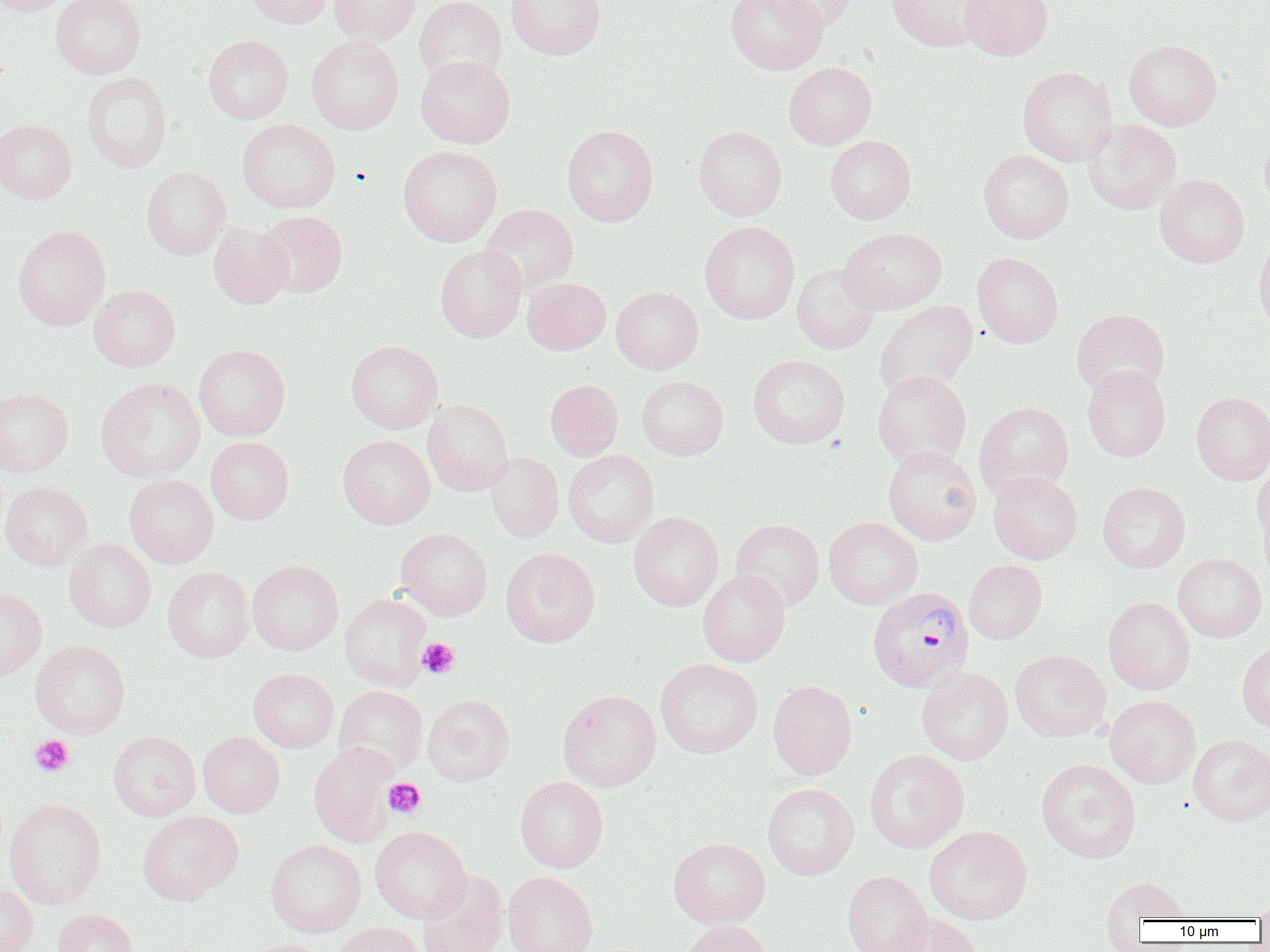
slide-level diagnosis = Plasmodium vivax
image size = 1270×952 pixels
preparation = thin blood smear
modality = optical microscopy
magnification = 1000x
Plasmodium vivax-infected red blood cell locations = approximate bounding boxes as named x1/y1/x2/y2 corners in pixels: (x1=867, y1=586, x2=974, y2=692)
uninfected red blood cell locations = approximate bounding boxes as named x1/y1/x2/y2 corners in pixels: (x1=0, y1=0, x2=74, y2=15), (x1=51, y1=0, x2=146, y2=78), (x1=245, y1=0, x2=334, y2=28), (x1=330, y1=0, x2=421, y2=45), (x1=414, y1=0, x2=506, y2=85), (x1=505, y1=0, x2=605, y2=60), (x1=726, y1=0, x2=828, y2=74), (x1=766, y1=0, x2=858, y2=31), (x1=887, y1=0, x2=992, y2=51), (x1=960, y1=0, x2=1053, y2=60), (x1=203, y1=35, x2=293, y2=124), (x1=307, y1=35, x2=404, y2=134), (x1=1124, y1=39, x2=1222, y2=130), (x1=415, y1=55, x2=515, y2=148), (x1=784, y1=61, x2=876, y2=149), (x1=1017, y1=66, x2=1117, y2=166), (x1=82, y1=72, x2=172, y2=172), (x1=0, y1=119, x2=77, y2=202), (x1=237, y1=119, x2=340, y2=213), (x1=1084, y1=119, x2=1182, y2=214), (x1=562, y1=124, x2=658, y2=225), (x1=694, y1=126, x2=787, y2=221), (x1=1260, y1=128, x2=1270, y2=215), (x1=825, y1=135, x2=916, y2=223), (x1=398, y1=145, x2=502, y2=247), (x1=978, y1=149, x2=1074, y2=243), (x1=141, y1=165, x2=231, y2=260), (x1=1155, y1=174, x2=1249, y2=267), (x1=481, y1=203, x2=578, y2=295), (x1=256, y1=211, x2=347, y2=297), (x1=699, y1=220, x2=800, y2=324), (x1=208, y1=222, x2=293, y2=309), (x1=13, y1=225, x2=110, y2=330), (x1=838, y1=227, x2=947, y2=314), (x1=1253, y1=233, x2=1270, y2=338), (x1=435, y1=245, x2=527, y2=342), (x1=972, y1=252, x2=1063, y2=347), (x1=792, y1=263, x2=880, y2=354), (x1=523, y1=277, x2=611, y2=354), (x1=89, y1=284, x2=180, y2=371), (x1=611, y1=286, x2=703, y2=374), (x1=875, y1=300, x2=978, y2=397), (x1=1071, y1=309, x2=1170, y2=398), (x1=346, y1=340, x2=443, y2=433), (x1=194, y1=344, x2=290, y2=441), (x1=748, y1=354, x2=850, y2=448), (x1=1082, y1=365, x2=1171, y2=461), (x1=872, y1=370, x2=971, y2=469), (x1=636, y1=376, x2=728, y2=459), (x1=96, y1=377, x2=205, y2=481), (x1=545, y1=379, x2=623, y2=461), (x1=0, y1=387, x2=74, y2=477), (x1=1191, y1=391, x2=1270, y2=484), (x1=422, y1=399, x2=513, y2=495), (x1=975, y1=401, x2=1073, y2=497), (x1=338, y1=435, x2=436, y2=528), (x1=206, y1=437, x2=294, y2=524), (x1=883, y1=445, x2=981, y2=545), (x1=563, y1=450, x2=659, y2=547), (x1=485, y1=451, x2=564, y2=543), (x1=1253, y1=458, x2=1269, y2=547), (x1=988, y1=471, x2=1082, y2=563), (x1=124, y1=474, x2=219, y2=568), (x1=0, y1=481, x2=93, y2=570), (x1=1097, y1=482, x2=1190, y2=572), (x1=1258, y1=497, x2=1270, y2=587), (x1=628, y1=511, x2=724, y2=611), (x1=823, y1=517, x2=922, y2=608), (x1=731, y1=518, x2=824, y2=611), (x1=396, y1=528, x2=492, y2=620), (x1=64, y1=538, x2=156, y2=632), (x1=500, y1=547, x2=600, y2=647), (x1=1173, y1=552, x2=1267, y2=642), (x1=247, y1=559, x2=343, y2=655), (x1=964, y1=559, x2=1047, y2=644), (x1=163, y1=566, x2=253, y2=662), (x1=698, y1=569, x2=791, y2=666), (x1=0, y1=587, x2=47, y2=681), (x1=339, y1=593, x2=432, y2=690), (x1=1104, y1=596, x2=1195, y2=695), (x1=1237, y1=638, x2=1270, y2=733), (x1=30, y1=639, x2=131, y2=738), (x1=1010, y1=649, x2=1111, y2=742), (x1=655, y1=658, x2=763, y2=758), (x1=916, y1=667, x2=1013, y2=764), (x1=249, y1=668, x2=338, y2=752), (x1=768, y1=680, x2=857, y2=779), (x1=334, y1=685, x2=428, y2=775), (x1=558, y1=689, x2=661, y2=791), (x1=423, y1=694, x2=515, y2=786), (x1=1105, y1=694, x2=1200, y2=788), (x1=108, y1=731, x2=200, y2=821), (x1=198, y1=732, x2=285, y2=817), (x1=1187, y1=734, x2=1270, y2=826), (x1=309, y1=743, x2=397, y2=847), (x1=865, y1=749, x2=969, y2=853), (x1=1036, y1=759, x2=1140, y2=863), (x1=515, y1=776, x2=608, y2=873), (x1=763, y1=783, x2=859, y2=880), (x1=5, y1=798, x2=106, y2=908), (x1=137, y1=811, x2=242, y2=905), (x1=925, y1=825, x2=1032, y2=924), (x1=370, y1=826, x2=471, y2=923), (x1=668, y1=837, x2=770, y2=928), (x1=266, y1=839, x2=366, y2=937), (x1=416, y1=870, x2=509, y2=952), (x1=503, y1=871, x2=598, y2=952), (x1=842, y1=871, x2=933, y2=952), (x1=1100, y1=875, x2=1193, y2=927), (x1=0, y1=882, x2=38, y2=952), (x1=1254, y1=892, x2=1270, y2=923), (x1=52, y1=907, x2=139, y2=952), (x1=884, y1=913, x2=985, y2=952), (x1=679, y1=920, x2=774, y2=952), (x1=329, y1=922, x2=425, y2=952), (x1=240, y1=939, x2=331, y2=952)
field of view = one of a larger specimen
platelet locations = approximate bounding boxes as named x1/y1/x2/y2 corners in pixels: (x1=417, y1=638, x2=460, y2=679), (x1=30, y1=734, x2=75, y2=777), (x1=383, y1=778, x2=426, y2=818)